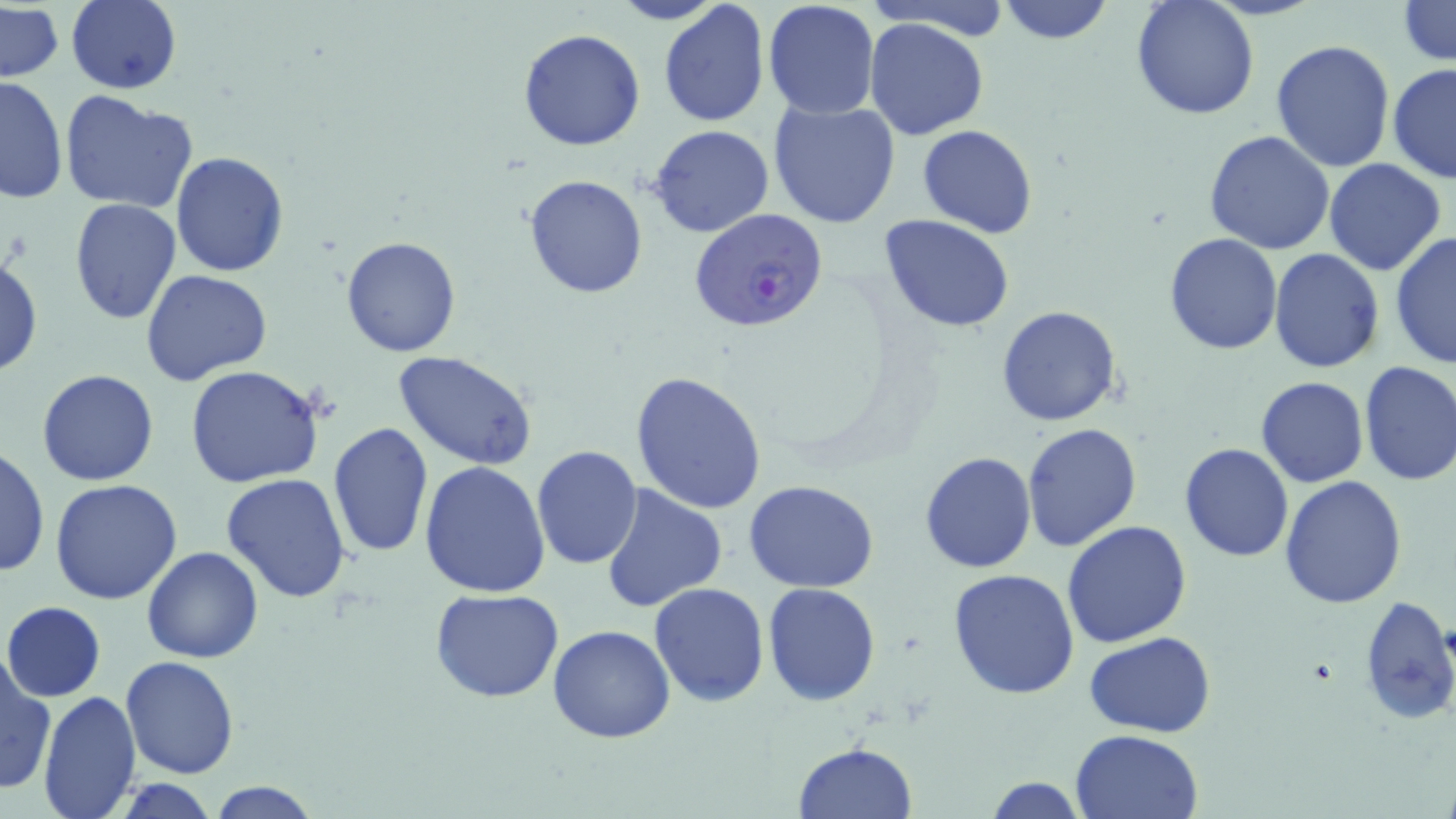

Approximate bounding boxes as named x1/y1/x2/y2 corners in pixels. Uninfected red blood cell locations: (x1=67, y1=0, x2=181, y2=93), (x1=608, y1=0, x2=725, y2=26), (x1=762, y1=0, x2=879, y2=119), (x1=863, y1=0, x2=1011, y2=38), (x1=999, y1=0, x2=1112, y2=45), (x1=1130, y1=0, x2=1259, y2=120), (x1=1397, y1=1, x2=1455, y2=68), (x1=658, y1=2, x2=770, y2=127), (x1=1, y1=5, x2=63, y2=84), (x1=864, y1=17, x2=991, y2=139), (x1=517, y1=28, x2=646, y2=151), (x1=1271, y1=39, x2=1397, y2=175), (x1=1387, y1=64, x2=1456, y2=185), (x1=0, y1=77, x2=68, y2=203), (x1=59, y1=90, x2=199, y2=214), (x1=767, y1=99, x2=899, y2=230), (x1=918, y1=124, x2=1037, y2=239), (x1=649, y1=125, x2=776, y2=239), (x1=1203, y1=130, x2=1336, y2=255), (x1=169, y1=152, x2=290, y2=276), (x1=1324, y1=158, x2=1448, y2=276), (x1=523, y1=173, x2=649, y2=298), (x1=68, y1=200, x2=182, y2=323), (x1=880, y1=214, x2=1015, y2=332), (x1=1389, y1=229, x2=1456, y2=370), (x1=1163, y1=231, x2=1284, y2=354), (x1=340, y1=236, x2=462, y2=357), (x1=1269, y1=248, x2=1384, y2=373), (x1=1, y1=252, x2=44, y2=380), (x1=141, y1=269, x2=273, y2=384), (x1=997, y1=305, x2=1123, y2=427), (x1=393, y1=350, x2=539, y2=471), (x1=1358, y1=361, x2=1455, y2=486), (x1=184, y1=365, x2=324, y2=488), (x1=36, y1=369, x2=158, y2=487), (x1=629, y1=369, x2=770, y2=513), (x1=1256, y1=376, x2=1368, y2=488), (x1=327, y1=421, x2=433, y2=560), (x1=1023, y1=424, x2=1142, y2=551), (x1=1179, y1=442, x2=1294, y2=562), (x1=532, y1=444, x2=642, y2=569), (x1=1, y1=445, x2=48, y2=580), (x1=919, y1=450, x2=1036, y2=574), (x1=420, y1=460, x2=550, y2=598), (x1=220, y1=474, x2=351, y2=606), (x1=1279, y1=476, x2=1407, y2=610), (x1=50, y1=480, x2=183, y2=605), (x1=744, y1=481, x2=878, y2=592), (x1=600, y1=484, x2=726, y2=612), (x1=1061, y1=521, x2=1192, y2=649), (x1=141, y1=546, x2=266, y2=663), (x1=948, y1=569, x2=1080, y2=700), (x1=649, y1=582, x2=770, y2=707), (x1=761, y1=582, x2=881, y2=706), (x1=430, y1=588, x2=564, y2=703), (x1=1358, y1=595, x2=1456, y2=726), (x1=3, y1=601, x2=106, y2=701), (x1=548, y1=625, x2=676, y2=743), (x1=1085, y1=631, x2=1216, y2=739), (x1=119, y1=655, x2=238, y2=777), (x1=1, y1=661, x2=55, y2=795), (x1=38, y1=689, x2=142, y2=819), (x1=1070, y1=728, x2=1203, y2=818), (x1=792, y1=743, x2=917, y2=819), (x1=982, y1=775, x2=1088, y2=818), (x1=207, y1=781, x2=321, y2=818). Plasmodium falciparum-infected red blood cell locations: (x1=690, y1=208, x2=829, y2=333). Slide-level diagnosis: Plasmodium falciparum. Captured at 1000x magnification. Image is 1456×819 pixels. Light microscopy. Thin blood film. May-Grünwald-Giemsa-stained preparation. Single field of view.